Mark where platelets are.
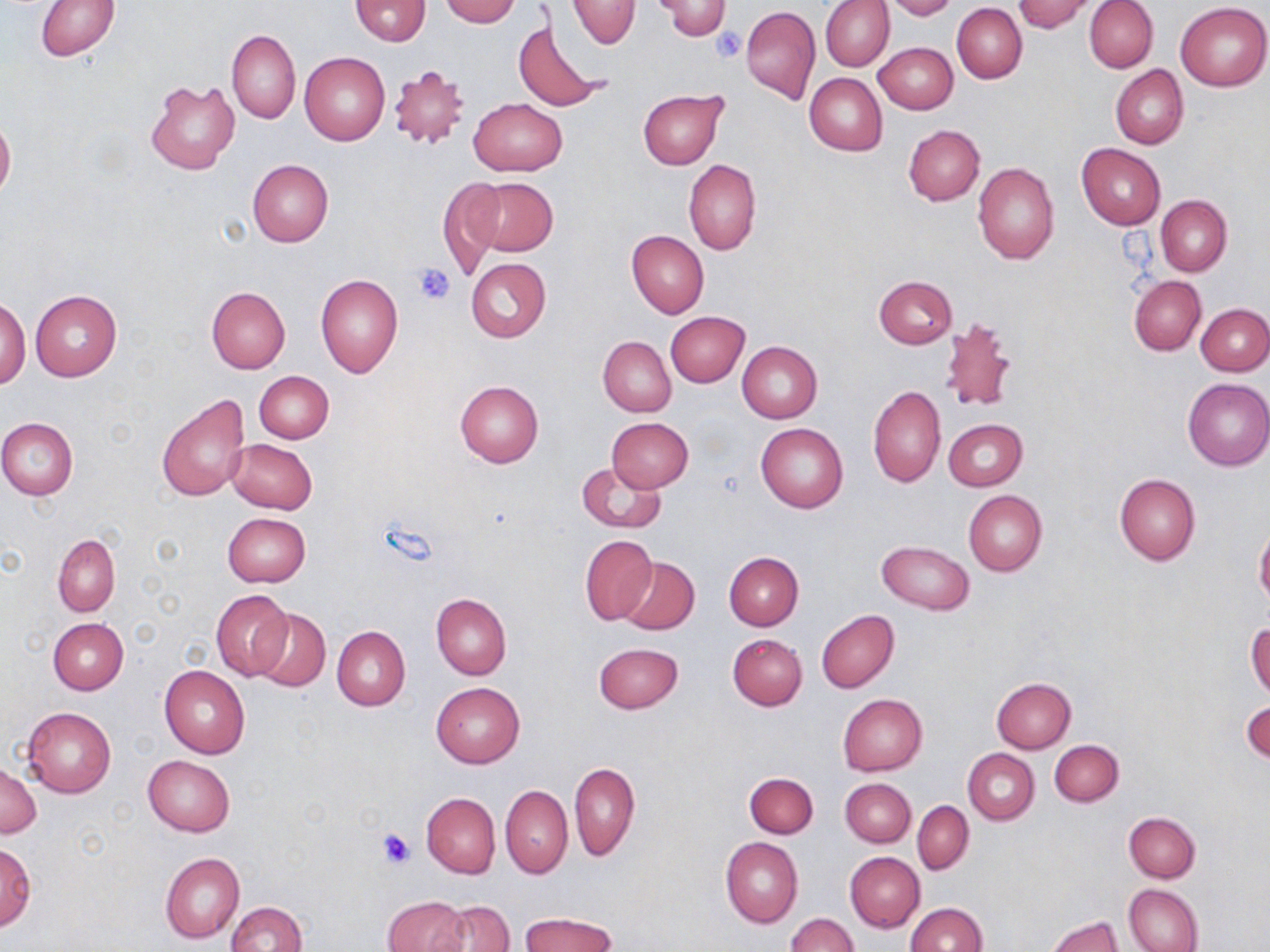

Approximate bounding boxes as (x1,y1)-(x2,y2) corner pairs in pixels.
Platelets: (711,26)-(746,63), (413,261)-(455,304), (376,827)-(416,869).

Uninfected red blood cell locations: (36,0)-(120,60), (350,0)-(430,44), (441,0)-(518,26), (567,0)-(640,48), (821,0)-(894,71), (885,0)-(957,19), (1013,0)-(1096,32), (1085,0)-(1158,73), (656,1)-(732,40), (1176,2)-(1270,91), (952,4)-(1027,83), (741,6)-(821,105), (513,19)-(607,112), (226,29)-(300,124), (874,42)-(957,114), (299,52)-(390,146), (1111,64)-(1189,150), (388,66)-(473,150), (804,74)-(887,156), (146,79)-(239,175), (638,89)-(727,168), (469,98)-(566,176), (0,118)-(15,198), (903,124)-(985,205), (1076,143)-(1166,229), (247,159)-(333,246), (684,159)-(762,256), (973,162)-(1059,264), (438,177)-(503,279), (469,178)-(557,257), (1157,195)-(1233,276), (627,230)-(708,318), (465,257)-(551,342), (315,273)-(402,377), (1128,275)-(1206,355), (873,276)-(957,349), (207,286)-(290,373), (30,290)-(122,382), (0,296)-(30,389), (1196,304)-(1270,376), (665,312)-(749,386), (939,318)-(1018,412), (598,337)-(676,416), (737,340)-(823,422), (254,371)-(334,444), (1182,377)-(1270,470), (454,379)-(544,468), (868,386)-(946,488), (156,392)-(250,501), (1,418)-(78,500), (607,418)-(693,493), (944,418)-(1027,491), (755,422)-(848,513), (226,437)-(318,514), (575,461)-(666,533), (1114,474)-(1200,566), (963,490)-(1047,577), (222,513)-(311,588), (1255,527)-(1270,609), (53,533)-(120,617), (579,534)-(657,626), (877,540)-(974,613), (724,552)-(803,630), (619,557)-(700,635), (211,590)-(291,680), (431,593)-(511,681), (251,607)-(331,693), (817,609)-(899,693), (48,617)-(127,694), (1246,622)-(1270,698), (332,625)-(410,710), (726,634)-(807,710), (594,642)-(683,713), (159,665)-(250,757), (992,677)-(1076,752), (432,683)-(524,768), (838,693)-(928,776), (1245,701)-(1270,764), (22,706)-(116,798), (1050,740)-(1123,806), (964,749)-(1039,824), (143,756)-(235,836), (0,762)-(39,837), (569,762)-(639,860), (745,772)-(818,837), (840,779)-(916,847), (500,783)-(572,878), (422,793)-(500,878), (913,801)-(974,875), (1124,811)-(1201,882), (720,837)-(803,928), (0,842)-(35,931), (160,852)-(244,943), (845,852)-(925,932), (1124,883)-(1203,952), (382,895)-(470,952), (438,900)-(515,952), (227,901)-(306,952), (905,903)-(987,952), (520,912)-(617,951), (786,914)-(858,952), (1045,915)-(1124,952). Slide-level diagnosis: no evidence of blood parasites. Captured at 1000x magnification. May-Grünwald-Giemsa stain. Image is 1270×952 pixels. Thin blood film. One field of a larger specimen. Light microscopy.